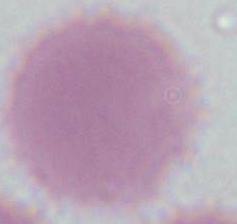

{
  "magnification": "1000x",
  "modality": "photomicrograph",
  "identification": "red blood cell"
}